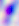
Micrograph. Toxoplasma gondii is shown. Captured at 400x magnification.